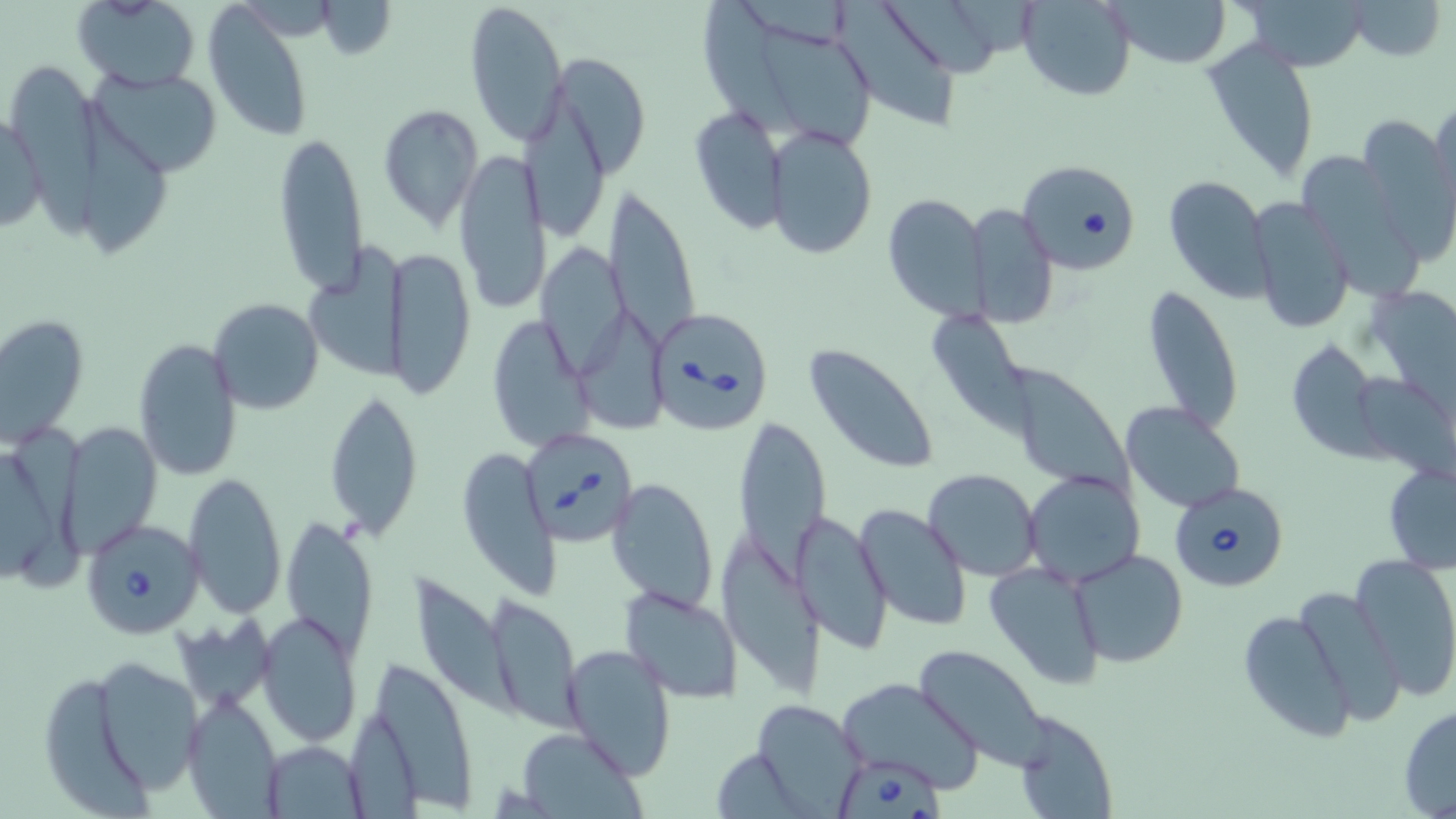

Summary:
  - Coordinate format: approximate bounding boxes as (x1, y1, x2, y2) in pixels
  - Babesia divergens-infected red blood cell locations: (1018, 157, 1141, 274), (653, 310, 767, 433), (522, 429, 637, 541), (1167, 480, 1289, 591), (80, 517, 206, 639), (832, 758, 946, 819)
  - Uninfected red blood cell locations: (72, 0, 202, 92), (465, 0, 569, 146), (1018, 0, 1135, 101), (1235, 0, 1373, 73), (1350, 0, 1446, 61), (702, 1, 803, 139), (1110, 1, 1230, 69), (203, 2, 316, 141), (834, 2, 965, 132), (888, 3, 1003, 83), (765, 29, 880, 145), (1203, 33, 1320, 185), (549, 57, 649, 175), (13, 62, 104, 245), (90, 74, 228, 179), (75, 95, 178, 257), (1427, 96, 1455, 226), (523, 99, 612, 242), (377, 105, 483, 228), (688, 105, 788, 233), (1, 109, 45, 237), (1356, 112, 1455, 262), (767, 126, 877, 260), (273, 132, 369, 298), (454, 145, 549, 316), (1293, 146, 1420, 307), (1161, 175, 1271, 301), (602, 187, 702, 358), (883, 193, 988, 321), (1249, 197, 1354, 336), (968, 203, 1058, 328), (533, 243, 635, 380), (308, 244, 414, 383), (384, 247, 477, 402), (1139, 284, 1244, 438), (1366, 286, 1454, 402), (207, 298, 325, 416), (582, 308, 672, 440), (1, 312, 88, 447), (485, 316, 591, 452), (938, 317, 1038, 438), (134, 338, 242, 482), (1286, 338, 1383, 458), (804, 343, 941, 475), (1001, 363, 1136, 498), (1357, 375, 1455, 482), (323, 388, 422, 540), (1122, 401, 1246, 513), (8, 417, 92, 592), (732, 421, 831, 588), (59, 422, 163, 554), (455, 448, 558, 596), (1382, 462, 1456, 572), (922, 469, 1040, 581), (1024, 470, 1145, 586), (182, 471, 286, 620), (609, 476, 719, 612), (854, 505, 971, 632), (795, 510, 893, 656), (281, 516, 379, 656), (718, 532, 822, 691), (1069, 548, 1190, 668), (1351, 553, 1456, 700), (986, 561, 1107, 689), (413, 574, 531, 721), (1297, 584, 1405, 726), (619, 586, 745, 701), (487, 594, 585, 731), (1236, 610, 1356, 739), (257, 613, 362, 749), (172, 619, 281, 708), (561, 644, 677, 778), (913, 646, 1049, 770), (367, 656, 477, 808), (90, 659, 206, 797), (835, 676, 984, 791), (45, 680, 161, 814), (181, 692, 280, 819), (752, 700, 868, 816), (1397, 703, 1456, 817), (1012, 711, 1117, 818), (515, 727, 645, 817), (261, 740, 368, 815)
  - Slide-level diagnosis: Babesia divergens
  - Modality: optical microscopy
  - Stain: May-Grünwald-Giemsa
  - Magnification: 1000x
  - Field of view: one of a larger specimen
  - Image size: 1456×819 pixels
  - Preparation: thin blood smear